Locate every blood parasite and identify its species.
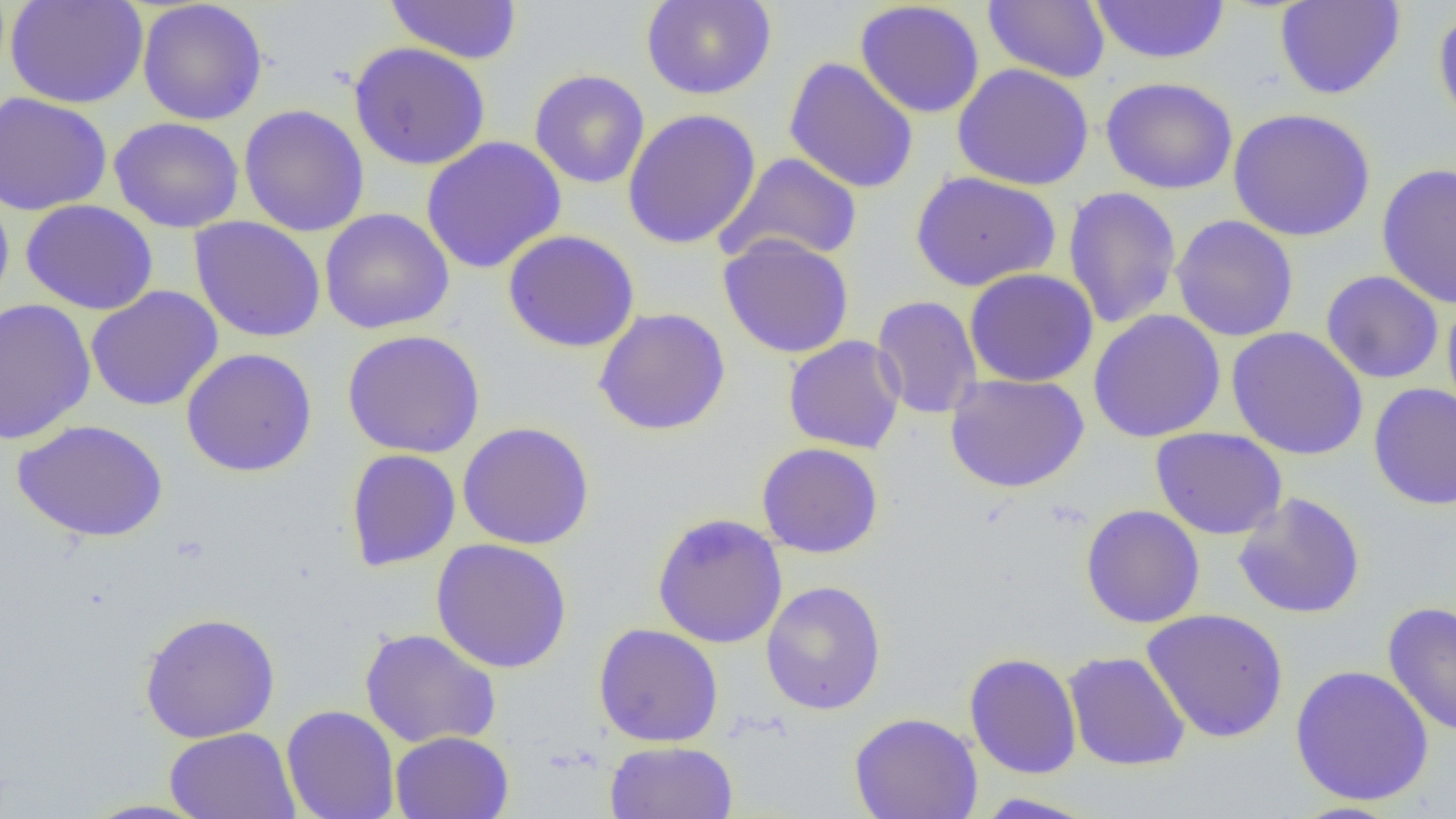

No blood parasites seen.

Approximate bounding boxes as named x1/y1/x2/y2 corners in pixels. Uninfected red blood cell locations: (x1=5, y1=0, x2=149, y2=109), (x1=384, y1=0, x2=523, y2=65), (x1=641, y1=0, x2=776, y2=100), (x1=982, y1=0, x2=1110, y2=83), (x1=1089, y1=0, x2=1231, y2=65), (x1=1274, y1=0, x2=1406, y2=100), (x1=137, y1=1, x2=268, y2=125), (x1=854, y1=1, x2=985, y2=119), (x1=1433, y1=6, x2=1456, y2=136), (x1=349, y1=41, x2=491, y2=171), (x1=784, y1=57, x2=920, y2=194), (x1=952, y1=64, x2=1094, y2=190), (x1=529, y1=69, x2=650, y2=189), (x1=1100, y1=76, x2=1239, y2=195), (x1=1, y1=92, x2=112, y2=215), (x1=238, y1=104, x2=370, y2=237), (x1=621, y1=108, x2=761, y2=250), (x1=1228, y1=108, x2=1376, y2=241), (x1=108, y1=116, x2=245, y2=233), (x1=421, y1=136, x2=566, y2=274), (x1=716, y1=152, x2=863, y2=265), (x1=1376, y1=162, x2=1456, y2=310), (x1=910, y1=170, x2=1061, y2=292), (x1=1063, y1=186, x2=1182, y2=329), (x1=0, y1=188, x2=14, y2=314), (x1=21, y1=199, x2=158, y2=315), (x1=319, y1=208, x2=455, y2=334), (x1=1170, y1=215, x2=1299, y2=342), (x1=189, y1=216, x2=327, y2=343), (x1=503, y1=229, x2=640, y2=353), (x1=718, y1=234, x2=855, y2=359), (x1=964, y1=268, x2=1099, y2=387), (x1=1321, y1=270, x2=1444, y2=384), (x1=85, y1=285, x2=223, y2=411), (x1=871, y1=294, x2=983, y2=420), (x1=1, y1=297, x2=97, y2=445), (x1=1441, y1=297, x2=1456, y2=425), (x1=593, y1=307, x2=731, y2=436), (x1=1087, y1=309, x2=1226, y2=443), (x1=1226, y1=326, x2=1368, y2=461), (x1=342, y1=329, x2=486, y2=459), (x1=783, y1=335, x2=906, y2=454), (x1=181, y1=347, x2=318, y2=477), (x1=945, y1=373, x2=1089, y2=493), (x1=1368, y1=382, x2=1456, y2=510), (x1=12, y1=419, x2=169, y2=543), (x1=457, y1=421, x2=594, y2=549), (x1=1150, y1=427, x2=1287, y2=539), (x1=756, y1=442, x2=884, y2=559), (x1=1176, y1=442, x2=1306, y2=594), (x1=345, y1=448, x2=461, y2=572), (x1=1233, y1=492, x2=1366, y2=619), (x1=1080, y1=505, x2=1206, y2=628), (x1=650, y1=512, x2=788, y2=649), (x1=431, y1=538, x2=572, y2=673), (x1=760, y1=580, x2=887, y2=715), (x1=1383, y1=601, x2=1456, y2=739), (x1=1141, y1=608, x2=1289, y2=744), (x1=139, y1=611, x2=280, y2=743), (x1=593, y1=623, x2=724, y2=747), (x1=360, y1=628, x2=501, y2=749), (x1=1062, y1=651, x2=1192, y2=771), (x1=964, y1=652, x2=1082, y2=779), (x1=1290, y1=665, x2=1434, y2=806), (x1=281, y1=705, x2=400, y2=819), (x1=849, y1=712, x2=983, y2=819), (x1=164, y1=727, x2=301, y2=819), (x1=389, y1=731, x2=514, y2=819), (x1=604, y1=741, x2=739, y2=819), (x1=972, y1=792, x2=1101, y2=818), (x1=78, y1=798, x2=215, y2=818). Slide-level diagnosis: no evidence of blood parasites. 1000x magnification. Thin blood smear. Optical microscopy. Image is 1456×819 pixels. One field of a larger specimen.